Assess for Plasmodium parasites.
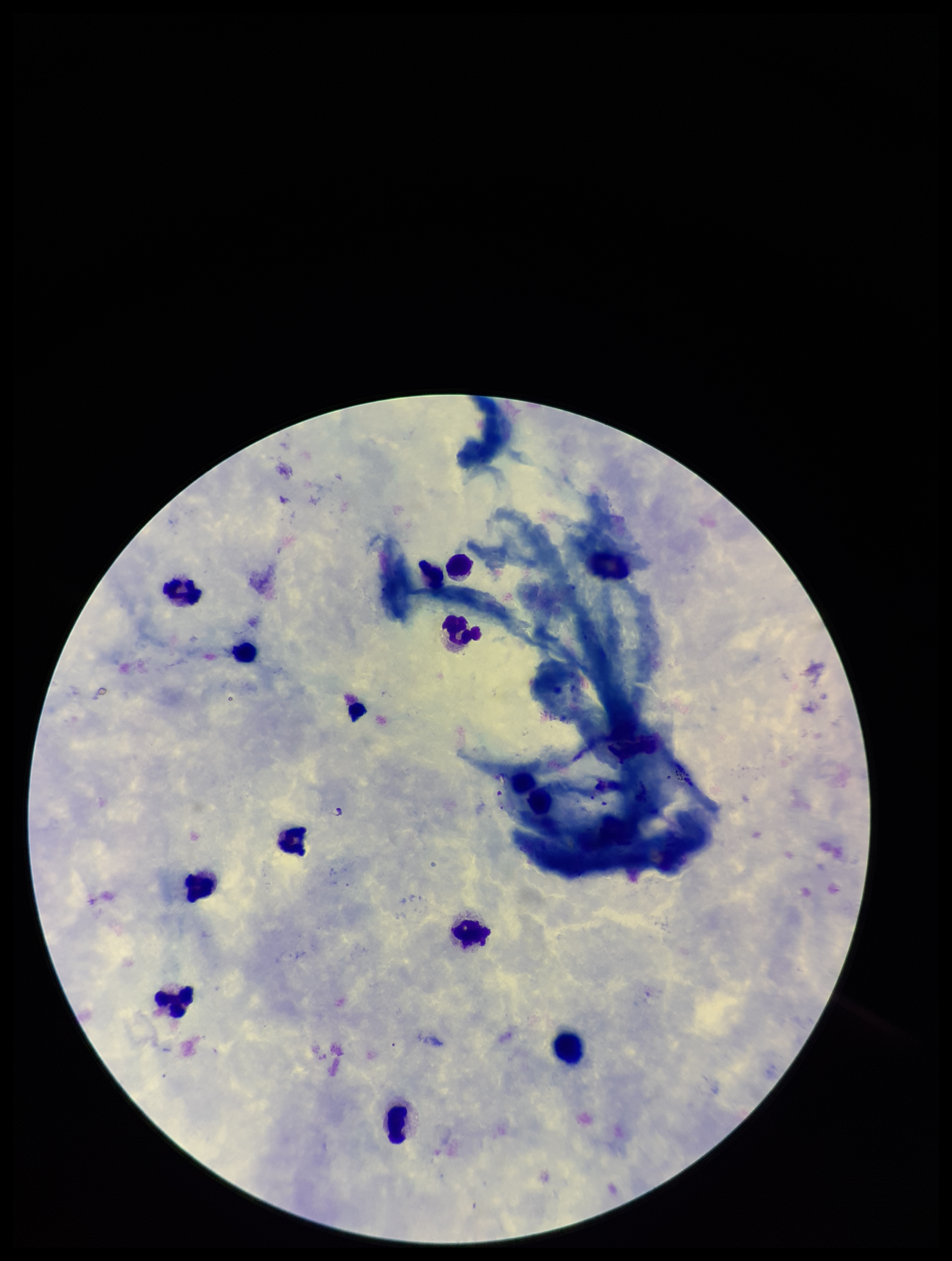
None seen.

Image is 952×1261 pixels. Stained with Giemsa. Photographed through the microscope eyepiece with a smartphone camera. Parasite count: 0. Patient malaria status: positive. Species reported for this patient: Plasmodium falciparum. Single field of view. Leukocyte count: 12. Preparation: thick.